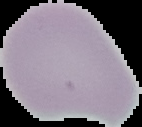
result = no Plasmodium parasites detected
image type = segmented cell region with the area outside set to black
image size = 142×127 pixels
preparation = thin blood smear